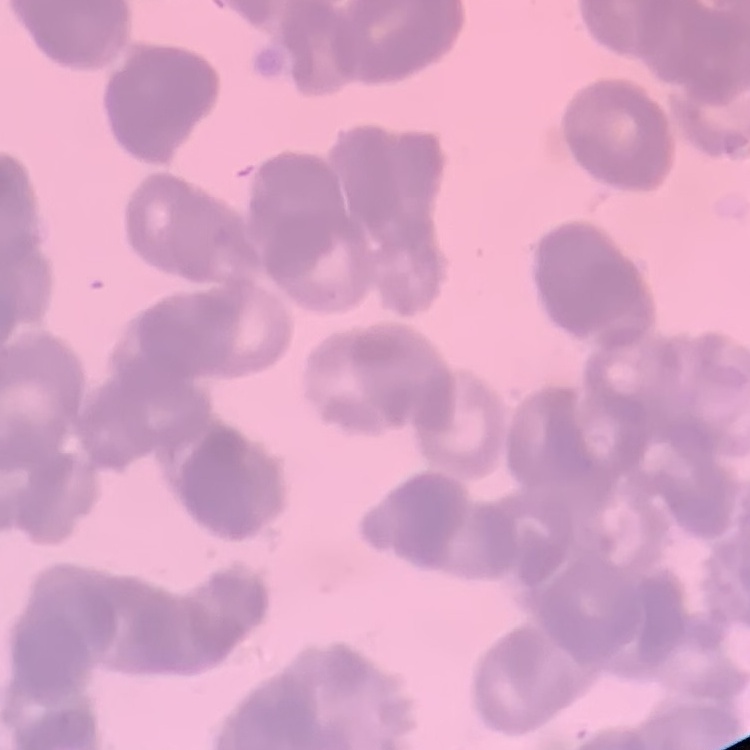

erythrocyte morphology = rouleaux formation
image type = square crop of a larger photomicrograph
stain = Field's or Giemsa
preparation = thin blood smear